Name the cell type shown.
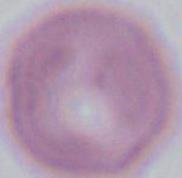

This is an erythrocyte.

Summary:
  - Magnification: 1000x
  - Modality: photomicrograph